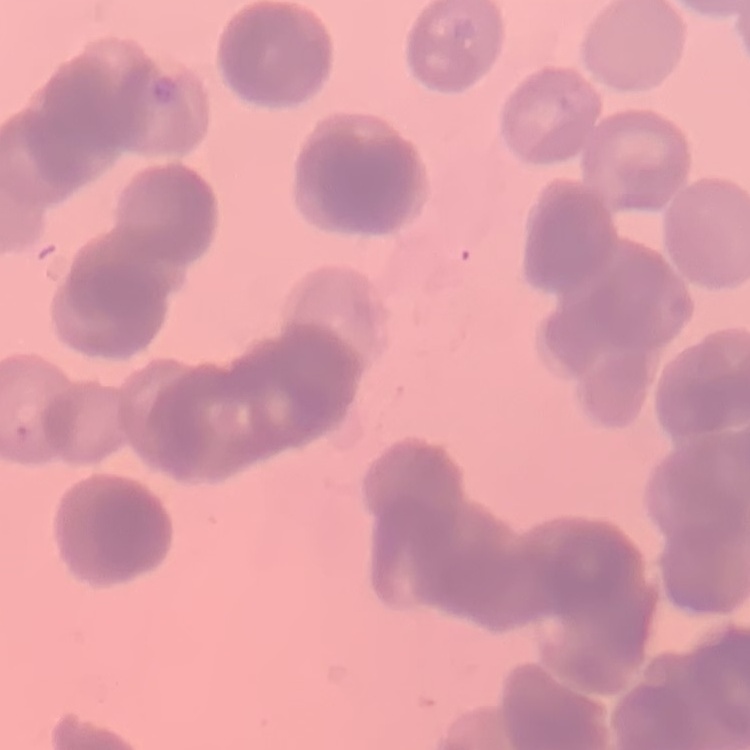

Summary:
  - Red blood cell morphology: rouleaux formation
  - Preparation: thin peripheral smear
  - Stain: Field's or Giemsa
  - Image type: one tile cut from a larger photomicrograph